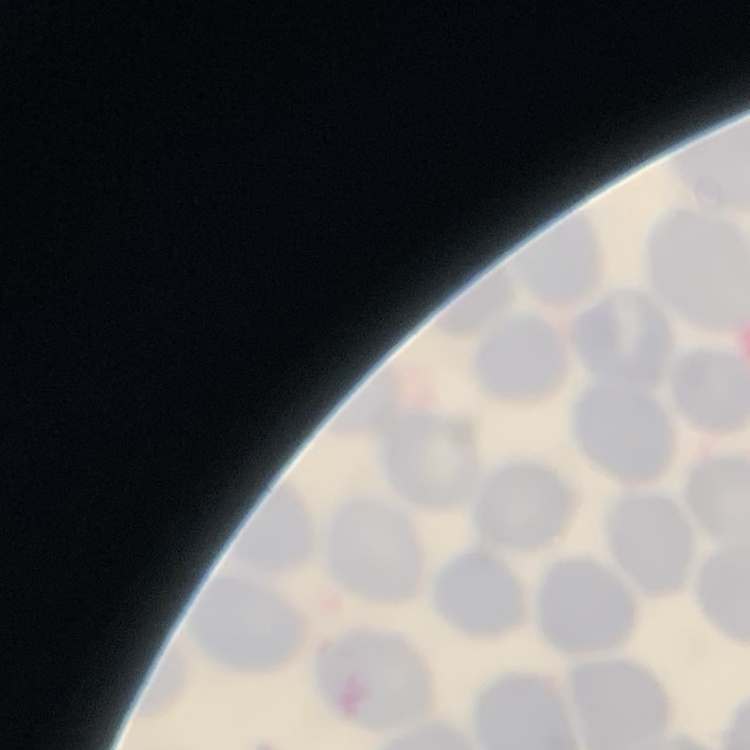

The red blood cells exhibit no rouleaux formation. Field's or Giemsa stain. Thin peripheral smear. One tile cut from a larger photomicrograph.